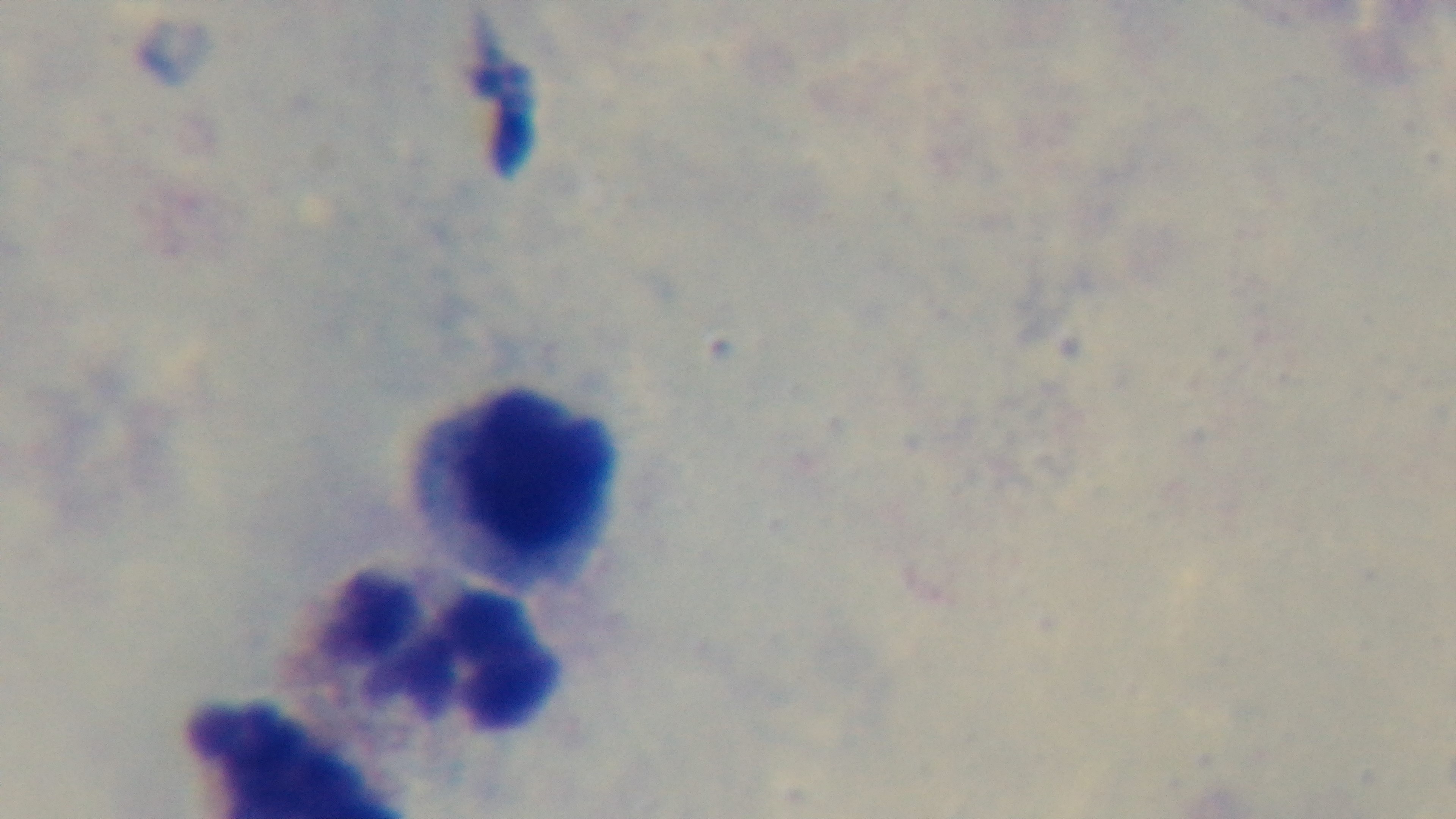

Summary:
  - Malaria status: uninfected
  - Modality: light microscopy
  - Objective: 100x oil immersion
  - Capture: mounted 4K digital camera
  - Preparation: thick
  - Field of view: one from the slide
  - Stain: Giemsa